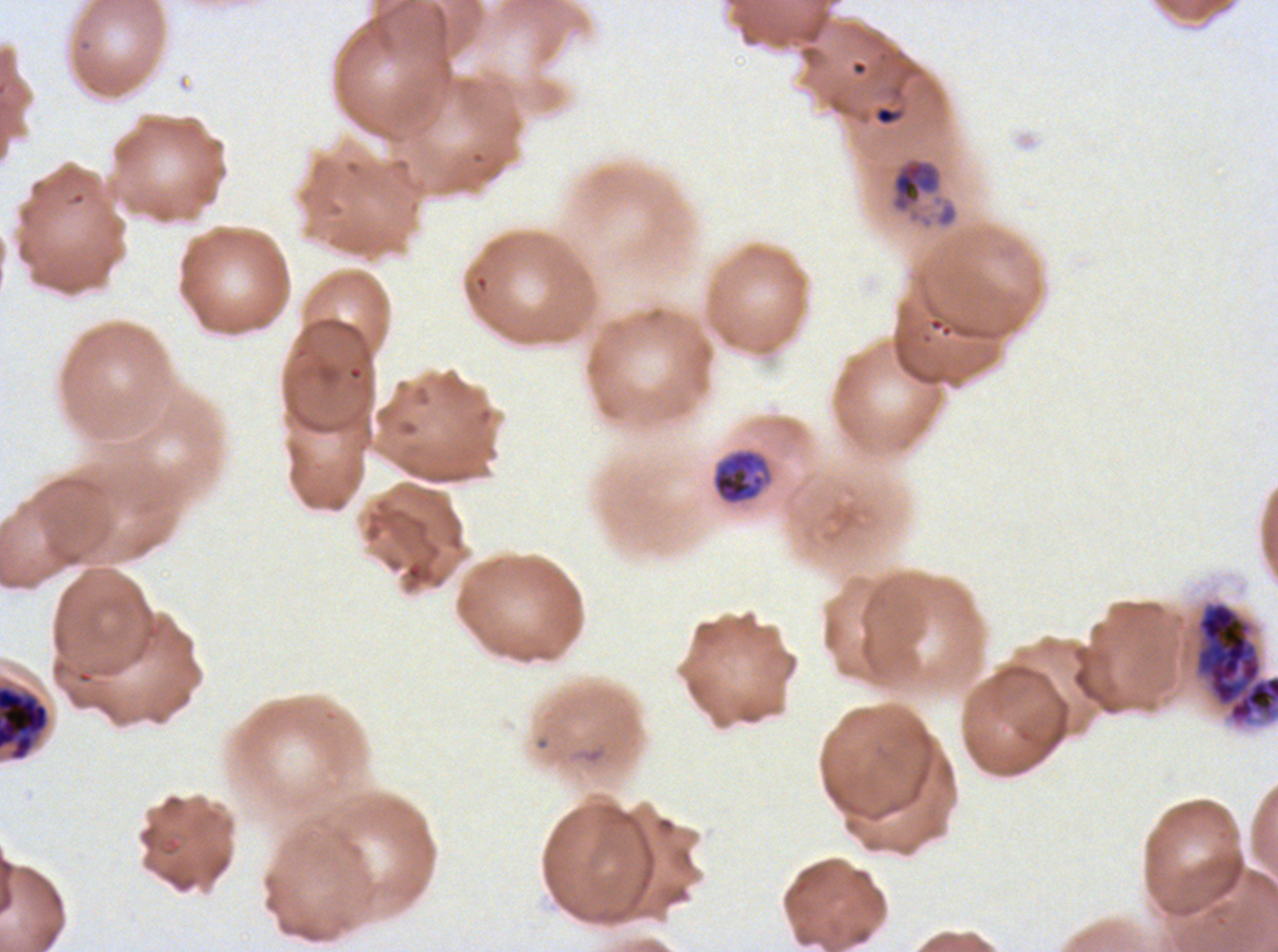

notation = approximate bounding boxes as (x1, y1, x2, y2) in pixels
late trophozoite locations = (891, 159, 940, 212)
mid trophozoite locations = (711, 448, 773, 507)
early schizont locations = (1193, 600, 1277, 728), (0, 683, 51, 762)
ring locations = (874, 105, 902, 126)
field of view = sub-image separated from a larger composite
specimen = P. falciparum from a patient in The Gambia, cultured ex vivo for 24 to 48 hours
preparation = thin blood smear
life-cycle stages observed = ring, mid trophozoite, late trophozoite, early schizont
stain = Giemsa
image size = 1278×952 pixels